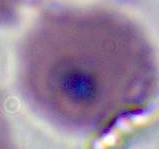
400x or 1000x magnification. Photomicrograph. A Plasmodium parasite is shown.